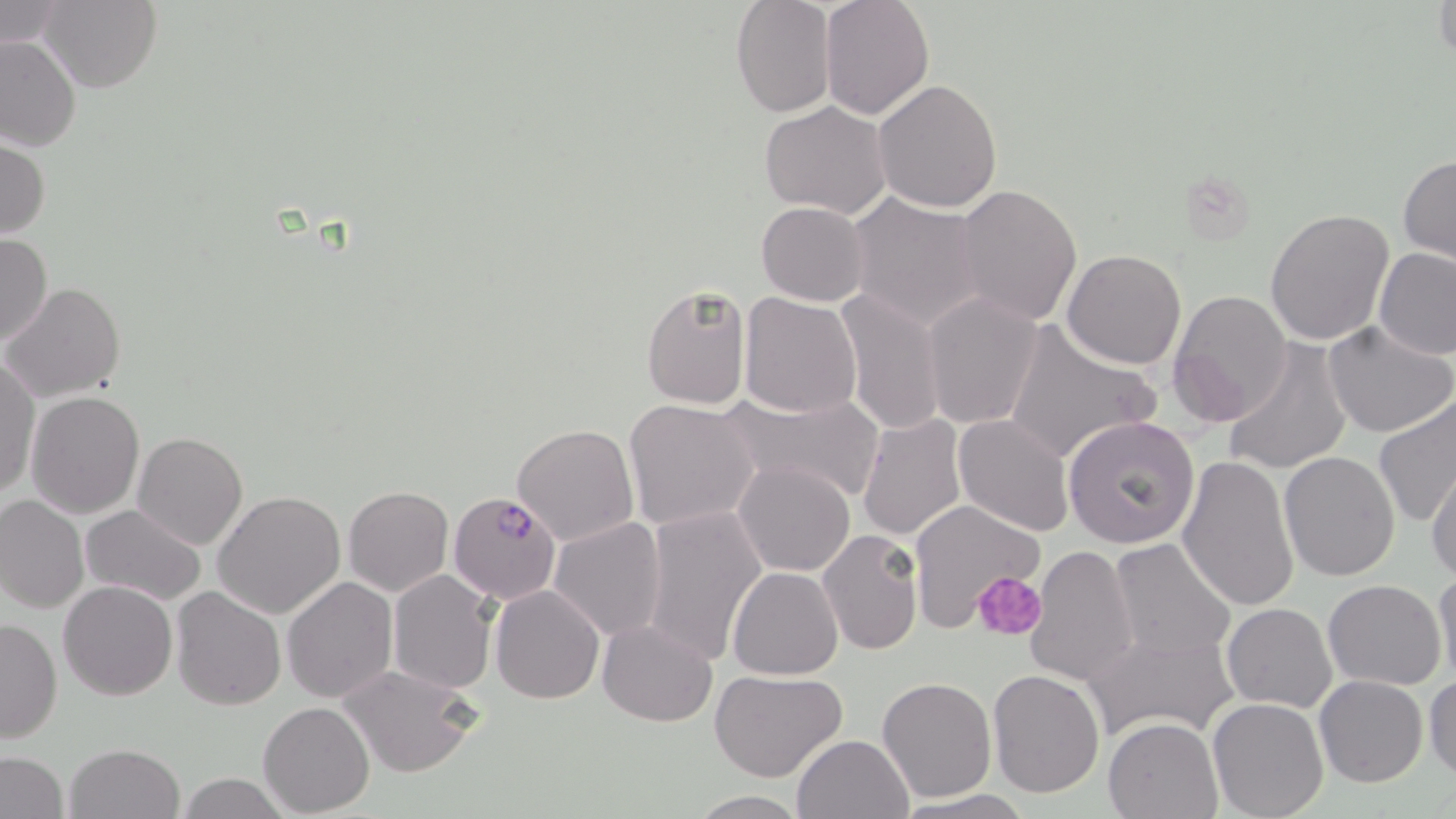

Approximate bounding boxes as (x1,y1)-(x2,y2) corner pairs in pixels. Plasmodium falciparum-infected red blood cell locations: (449,492)-(562,606). Platelet locations: (975,571)-(1048,641). Uninfected red blood cell locations: (40,0)-(162,94), (730,0)-(837,119), (819,0)-(934,121), (1432,0)-(1454,64), (0,1)-(70,52), (0,35)-(81,153), (873,80)-(1004,213), (758,100)-(892,220), (0,136)-(50,240), (1398,154)-(1456,267), (953,184)-(1083,327), (847,192)-(987,331), (755,200)-(869,305), (1265,206)-(1397,345), (0,233)-(52,347), (1373,247)-(1456,360), (1061,248)-(1187,369), (640,281)-(752,411), (4,282)-(127,403), (836,288)-(944,437), (1168,289)-(1293,427), (739,292)-(862,419), (922,293)-(1046,431), (1001,321)-(1160,466), (1324,321)-(1456,438), (1224,338)-(1352,477), (1,359)-(39,498), (722,387)-(882,504), (26,390)-(144,518), (1373,397)-(1456,529), (624,398)-(759,532), (857,412)-(968,541), (953,413)-(1074,537), (1062,413)-(1199,549), (512,424)-(640,547), (132,431)-(248,549), (1279,450)-(1401,581), (1177,453)-(1302,613), (734,460)-(856,577), (1426,462)-(1456,584), (342,486)-(453,597), (212,490)-(346,617), (0,494)-(88,614), (905,498)-(1046,634), (79,504)-(205,606), (641,505)-(766,666), (549,516)-(667,643), (817,529)-(924,656), (498,532)-(656,690), (1108,537)-(1236,663), (1025,545)-(1139,686), (727,566)-(845,679), (1432,567)-(1456,685), (387,570)-(499,695), (281,576)-(399,704), (1324,578)-(1448,690), (58,581)-(178,700), (489,584)-(605,705), (169,587)-(286,711), (1229,591)-(1446,708), (1222,603)-(1338,713), (0,616)-(62,744), (597,619)-(719,726), (1085,626)-(1240,743), (336,663)-(483,780), (987,668)-(1105,797), (710,670)-(847,784), (1425,673)-(1456,782), (878,676)-(998,803), (1314,676)-(1428,788), (1207,698)-(1329,819), (259,701)-(375,816), (1103,717)-(1223,818), (792,733)-(914,818), (64,743)-(184,819), (1,752)-(68,819), (174,772)-(292,818), (893,789)-(1037,819), (688,791)-(808,818). Slide-level diagnosis: Plasmodium falciparum. Thin blood smear. Optical microscopy. May-Grünwald-Giemsa stain. Image is 1456×819 pixels. 1000x magnification. Single field of view.